Locate every Plasmodium parasite.
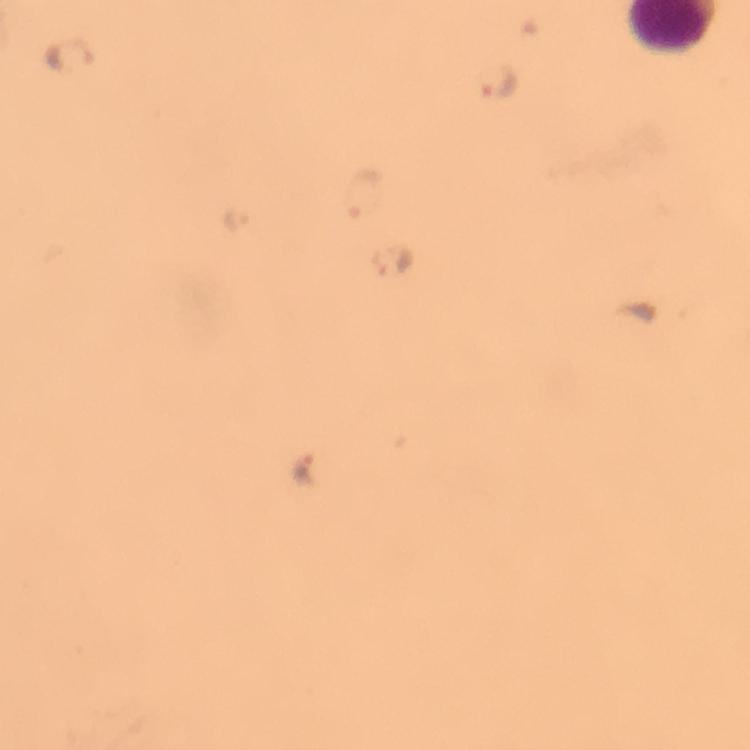
Approximate centers as (x, y) in pixels.
Plasmodium parasites: (496, 81), (364, 193), (237, 218), (305, 467).

Summary:
  - Image size: 750×750 pixels
  - Preparation: thick blood film
  - Cropped from: a single field of view
  - Capture: smartphone mounted on the microscope
  - Immersion oil: used
  - Context: from a malaria diagnostic workup
  - Magnification: 100x
  - Stain: Giemsa